Give the extent of all uninfected red blood cells.
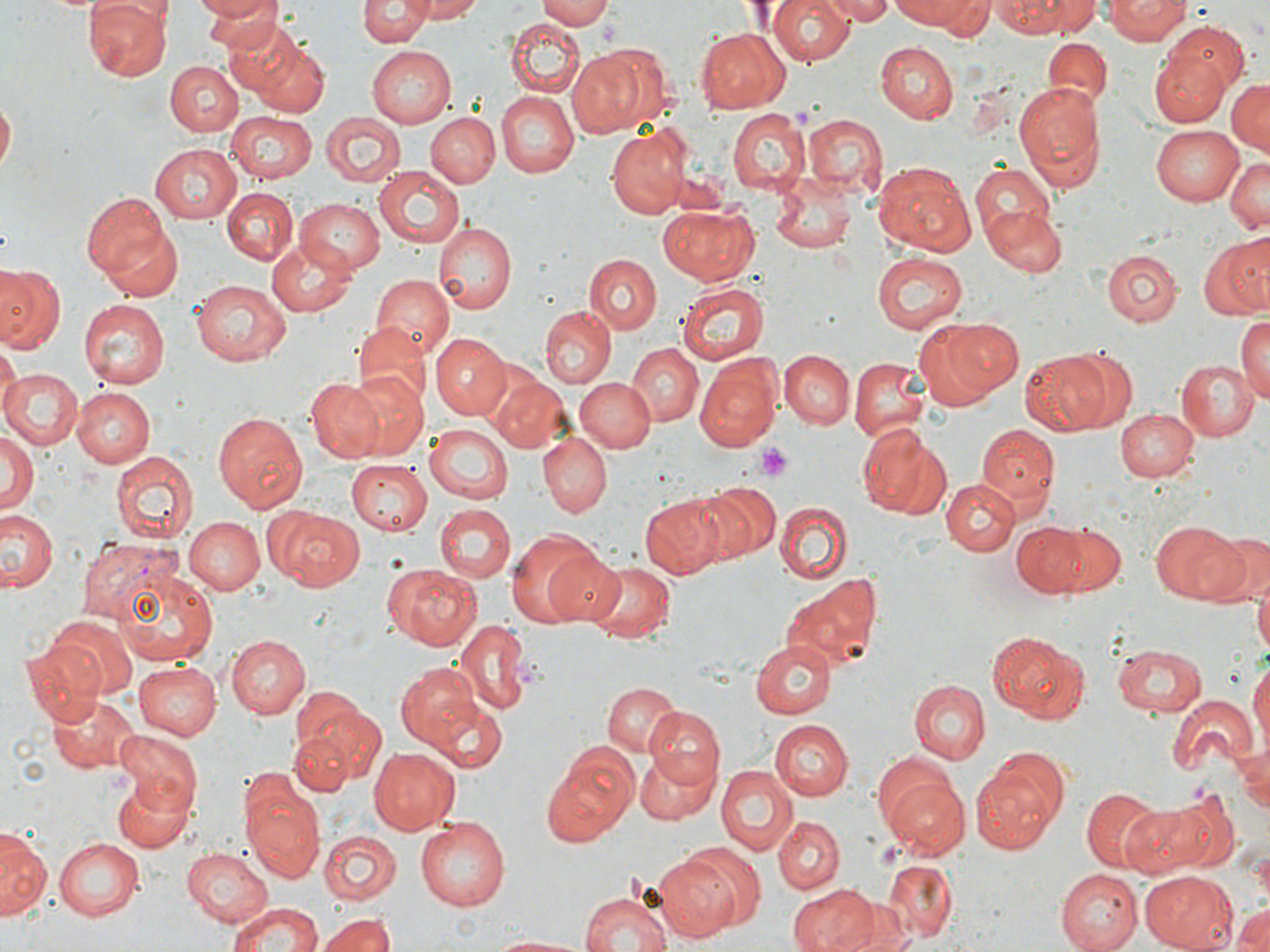
Approximate bounding boxes as (x1,y1)-(x2,y2) corner pairs in pixels.
Uninfected red blood cells: (86,0)-(171,80), (190,0)-(278,23), (199,0)-(282,50), (361,0)-(431,45), (411,0)-(488,21), (538,0)-(615,28), (765,0)-(855,66), (825,0)-(898,24), (888,0)-(980,28), (918,0)-(995,38), (1042,0)-(1103,34), (1105,0)-(1191,44), (991,1)-(1078,37), (219,19)-(307,97), (507,19)-(585,97), (1159,21)-(1251,101), (695,28)-(790,112), (1043,37)-(1110,107), (245,38)-(330,116), (874,42)-(957,123), (364,44)-(454,128), (1149,44)-(1230,126), (566,47)-(652,137), (166,61)-(242,137), (1226,77)-(1268,155), (1014,81)-(1106,191), (496,91)-(578,178), (0,95)-(16,181), (428,104)-(567,186), (727,109)-(811,195), (227,111)-(317,183), (319,112)-(403,189), (427,112)-(499,188), (804,114)-(886,197), (1151,124)-(1245,205), (607,126)-(696,217), (149,144)-(242,222), (1223,156)-(1270,235), (872,160)-(977,258), (969,160)-(1056,243), (373,166)-(466,248), (770,172)-(856,255), (222,188)-(298,264), (82,192)-(175,280), (295,198)-(386,273), (658,206)-(760,287), (983,207)-(1067,278), (435,221)-(517,311), (101,223)-(182,301), (1198,234)-(1270,321), (266,241)-(356,318), (1103,249)-(1182,326), (872,251)-(971,335), (585,253)-(661,334), (3,263)-(72,438), (0,265)-(64,354), (370,274)-(453,358), (192,280)-(291,367), (678,281)-(769,364), (78,299)-(169,390), (538,305)-(616,388), (1237,313)-(1270,405), (914,317)-(1018,407), (353,323)-(428,398), (428,333)-(510,419), (628,344)-(704,424), (0,346)-(19,420), (1020,349)-(1117,435), (779,350)-(854,429), (1068,351)-(1136,427), (1176,358)-(1256,441), (850,359)-(928,442), (693,363)-(781,453), (0,368)-(82,451), (347,372)-(428,457), (490,375)-(573,453), (304,377)-(385,462), (576,378)-(655,453), (72,387)-(155,468), (1116,408)-(1198,482), (212,410)-(307,512), (424,423)-(514,503), (977,424)-(1060,507), (858,429)-(952,520), (0,430)-(38,521), (539,434)-(612,517), (112,450)-(197,545), (346,460)-(433,534), (942,478)-(1018,555), (694,483)-(778,562), (641,493)-(733,578), (775,502)-(853,584), (436,504)-(514,584), (267,507)-(366,586), (0,508)-(57,593), (185,517)-(264,595), (1152,520)-(1250,605), (1011,522)-(1086,599), (1044,522)-(1126,597), (1206,528)-(1269,607), (506,532)-(599,628), (538,545)-(625,626), (579,556)-(675,643), (382,563)-(482,650), (115,566)-(217,667), (1255,571)-(1269,665), (783,577)-(881,673), (44,615)-(138,698), (454,618)-(530,716), (991,631)-(1087,722), (227,634)-(310,718), (752,639)-(837,717), (18,640)-(104,722), (1113,641)-(1209,718), (135,662)-(222,740), (394,662)-(487,754), (1249,662)-(1270,755), (908,680)-(988,764), (602,682)-(683,757), (290,684)-(379,780), (421,690)-(509,773), (48,692)-(137,774), (1168,694)-(1256,776), (646,707)-(724,788), (770,720)-(852,800), (288,725)-(358,797), (114,729)-(202,812), (1231,737)-(1270,820), (368,746)-(460,835), (542,749)-(636,846), (633,749)-(717,824), (971,755)-(1065,855), (714,764)-(795,853), (881,776)-(971,861), (109,777)-(195,854), (240,777)-(324,882), (1081,787)-(1164,870), (1133,791)-(1235,876), (773,815)-(843,894), (417,817)-(511,910), (0,826)-(50,919), (320,830)-(401,903), (56,838)-(144,919), (184,848)-(272,926), (651,852)-(740,940), (882,859)-(957,944), (1058,868)-(1144,952), (1140,870)-(1241,951), (789,884)-(877,952), (579,891)-(670,952), (842,902)-(916,952), (229,903)-(323,952), (1231,903)-(1270,952), (319,911)-(398,952), (485,933)-(593,951).

slide-level diagnosis = Plasmodium vivax
stain = May-Grünwald-Giemsa
image size = 1270×952 pixels
field of view = one of a larger specimen
magnification = 1000x
preparation = thin blood film
Plasmodium vivax-infected red blood cell locations = approximate bounding boxes as (x1,y1)-(x2,y2) corner pairs in pixels: (78,538)-(179,628)
platelet locations = approximate bounding boxes as (x1,y1)-(x2,y2) corner pairs in pixels: (755,443)-(794,481)
modality = optical microscopy